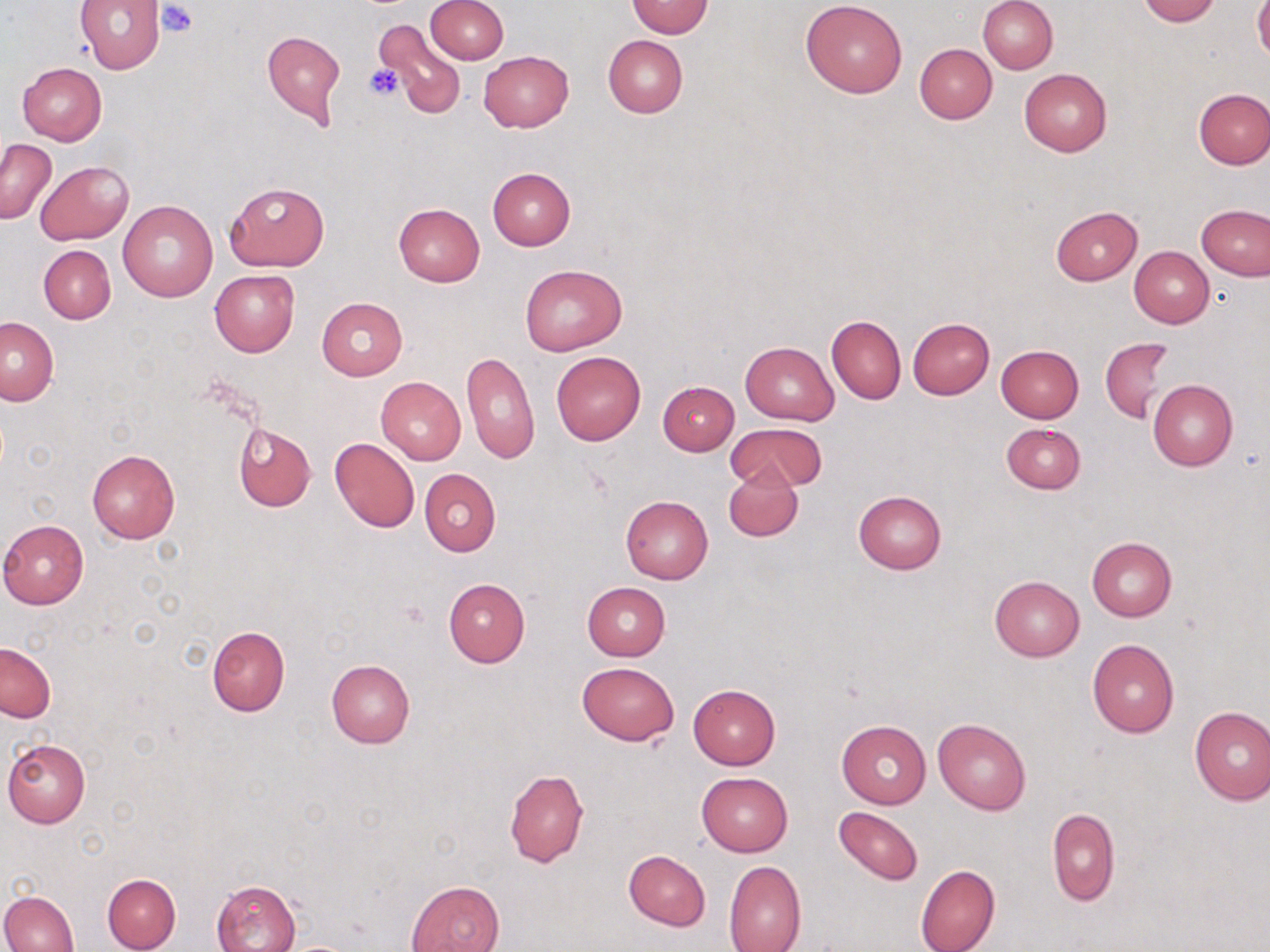
Approximate bounding boxes as (x1,y1)-(x2,y2) corner pairs in pixels. Uninfected red blood cell locations: (74,0)-(165,73), (424,0)-(508,64), (979,0)-(1058,74), (1137,0)-(1218,25), (801,1)-(908,98), (625,2)-(714,38), (1253,2)-(1270,63), (376,19)-(465,119), (261,31)-(346,126), (603,35)-(688,117), (914,44)-(996,123), (479,51)-(573,132), (17,63)-(107,145), (1019,68)-(1112,155), (1194,89)-(1270,168), (1,138)-(55,224), (36,161)-(133,245), (487,167)-(576,250), (225,180)-(330,271), (117,200)-(218,302), (393,203)-(486,287), (1197,204)-(1270,281), (1050,207)-(1143,286), (39,245)-(115,323), (1129,247)-(1213,328), (520,265)-(626,356), (210,270)-(299,357), (317,297)-(407,380), (826,314)-(906,404), (1,316)-(58,406), (907,318)-(995,400), (1101,338)-(1174,423), (740,341)-(840,425), (995,344)-(1084,424), (462,350)-(540,465), (552,352)-(646,445), (376,375)-(467,465), (1148,378)-(1238,471), (658,381)-(739,455), (1001,422)-(1085,494), (233,424)-(316,511), (727,424)-(827,492), (330,437)-(420,532), (86,449)-(179,543), (724,467)-(804,542), (419,468)-(500,557), (854,491)-(946,574), (619,495)-(713,583), (0,520)-(88,609), (1086,537)-(1177,622), (988,576)-(1084,662), (444,578)-(530,667), (581,583)-(670,661), (207,626)-(290,715), (1086,638)-(1180,737), (1,642)-(55,723), (326,658)-(414,748), (578,661)-(678,746), (688,684)-(780,769), (1188,706)-(1270,805), (933,717)-(1031,814), (837,720)-(931,808), (2,739)-(90,828), (503,769)-(589,868), (697,771)-(793,856), (831,805)-(924,888), (1047,808)-(1120,905), (623,850)-(711,931), (723,860)-(806,952), (915,864)-(1000,952), (102,874)-(180,952), (212,880)-(300,952), (407,880)-(505,952), (0,890)-(79,952). Platelet locations: (157,3)-(197,37), (365,63)-(403,100). Slide-level diagnosis: no evidence of blood parasites. Light microscopy. Image is 1270×952 pixels. One field of a larger specimen. 1000x magnification. Thin blood film. May-Grünwald-Giemsa stain.